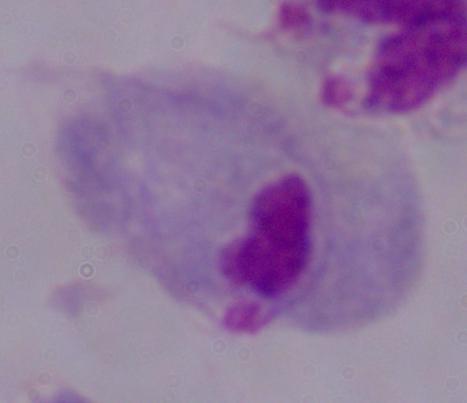

Photomicrograph. Captured at 1000x magnification. A trichomonad is shown.